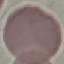
Summary:
  - Malaria status: uninfected
  - Capture: smartphone camera at the microscope eyepiece
  - Stain: Giemsa
  - Preparation: thin blood smear
  - Image type: cell patch, automatically extracted from a larger field of view and resized to 64 × 64 pixels